Report the malaria status of this cell.
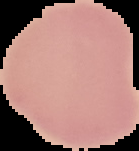
Uninfected.

Summary:
  - Image type: segmented cell region with the area outside set to black
  - Image size: 139×151 pixels
  - Preparation: thin blood smear